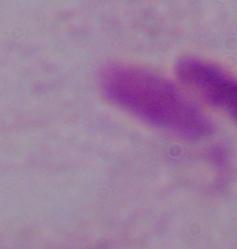

Summary:
  - Modality: micrograph
  - Identification: trichomonad
  - Magnification: 1000x